Identify the cell.
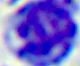

A leukocyte.

{
  "magnification": "400x",
  "modality": "micrograph"
}